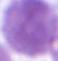
Summary:
  - Modality: photomicrograph
  - Identification: red blood cell
  - Magnification: 1000x